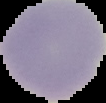
preparation: thin blood smear
image_size: 106×103 pixels
result: no malaria parasites detected
image_type: segmented cell region with the area outside set to black